Locate every leukocyte (white blood cell).
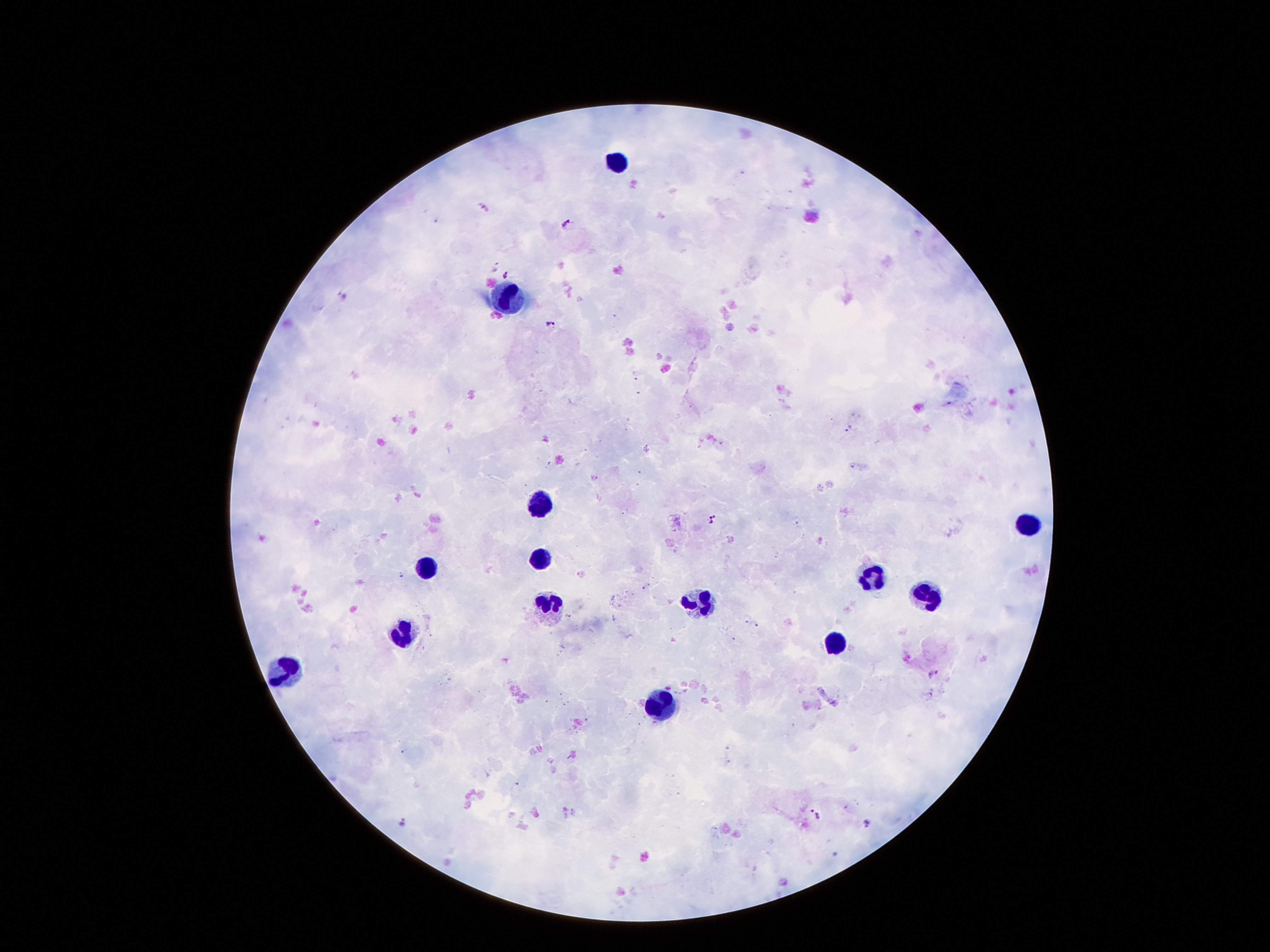
Approximate centers as {x, y} in pixels.
Leukocytes: {617, 160}, {510, 297}, {535, 503}, {1028, 522}, {541, 560}, {426, 564}, {873, 578}, {928, 599}, {699, 604}, {549, 608}, {403, 626}, {839, 639}, {283, 671}, {663, 704}.

Malaria parasite locations: {482, 207}, {569, 222}, {493, 265}, {505, 273}, {551, 323}, {947, 404}, {849, 429}, {712, 517}, {401, 576}, {569, 616}, {745, 617}, {757, 625}, {933, 674}, {517, 783}, {813, 813}, {404, 821}, {867, 824}. Giemsa stain. Patient malaria status: positive for Plasmodium falciparum. Single field of view. Photographed through the microscope eyepiece with a smartphone camera. Thick peripheral-blood smear. Image is 1270×952 pixels. 100x magnification.